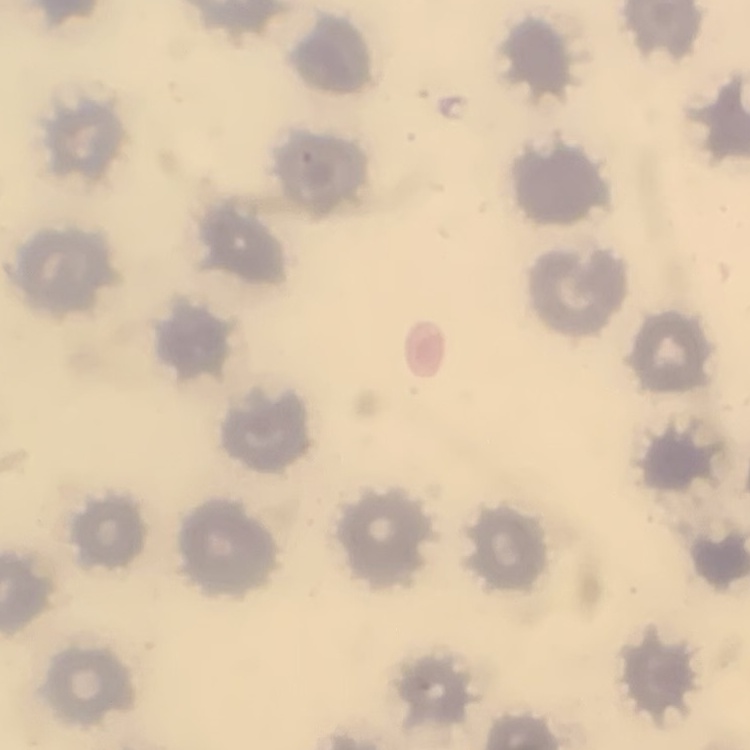
Summary:
  - Erythrocyte morphology: no rouleaux formation
  - Stain: Field's or Giemsa
  - Preparation: thin peripheral smear
  - Image type: square crop of a larger photomicrograph